Locate every blood parasite and identify its species.
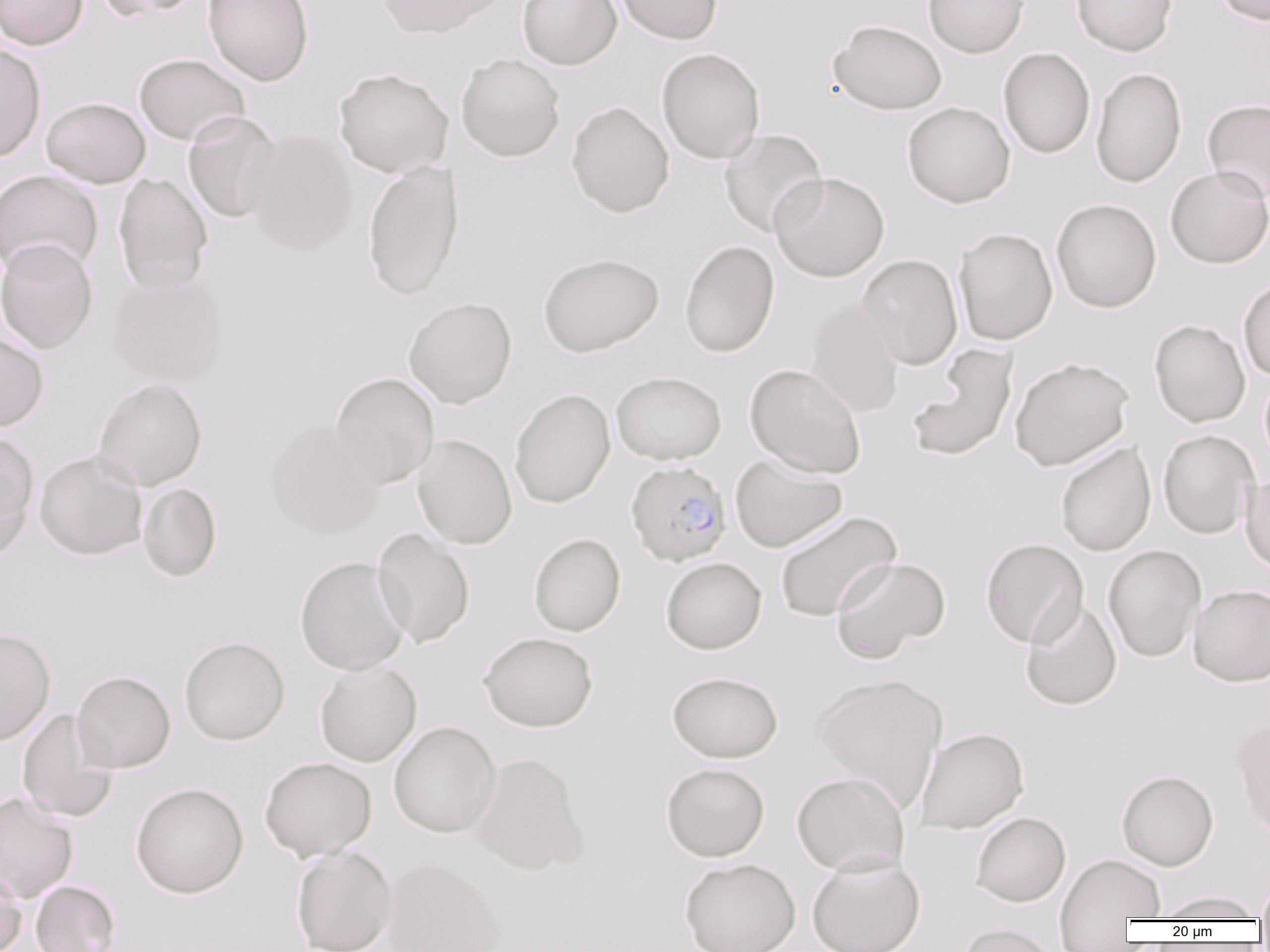

Approximate bounding boxes as named x1/y1/x2/y2 corners in pixels.
Plasmodium falciparum-infected red blood cells: (x1=625, y1=460, x2=732, y2=566).
No Plasmodium ovale, Plasmodium malariae, Plasmodium vivax, Babesia divergens, or Trypanosoma brucei observed.

Uninfected red blood cell locations: (x1=0, y1=0, x2=87, y2=50), (x1=94, y1=0, x2=204, y2=21), (x1=202, y1=0, x2=315, y2=86), (x1=376, y1=0, x2=503, y2=38), (x1=517, y1=0, x2=622, y2=70), (x1=612, y1=0, x2=723, y2=44), (x1=923, y1=0, x2=1029, y2=58), (x1=1071, y1=0, x2=1178, y2=56), (x1=1212, y1=0, x2=1270, y2=26), (x1=828, y1=19, x2=947, y2=114), (x1=0, y1=43, x2=46, y2=163), (x1=656, y1=47, x2=766, y2=164), (x1=998, y1=47, x2=1095, y2=159), (x1=134, y1=53, x2=250, y2=145), (x1=455, y1=54, x2=566, y2=162), (x1=1090, y1=67, x2=1187, y2=188), (x1=333, y1=68, x2=453, y2=178), (x1=41, y1=97, x2=150, y2=188), (x1=1202, y1=98, x2=1270, y2=203), (x1=566, y1=101, x2=675, y2=218), (x1=902, y1=102, x2=1015, y2=208), (x1=183, y1=111, x2=283, y2=223), (x1=245, y1=128, x2=357, y2=256), (x1=719, y1=129, x2=828, y2=237), (x1=362, y1=159, x2=464, y2=300), (x1=1164, y1=167, x2=1270, y2=269), (x1=0, y1=169, x2=103, y2=278), (x1=770, y1=171, x2=890, y2=281), (x1=113, y1=173, x2=213, y2=294), (x1=1051, y1=198, x2=1162, y2=313), (x1=953, y1=228, x2=1058, y2=346), (x1=0, y1=238, x2=99, y2=354), (x1=679, y1=240, x2=779, y2=358), (x1=537, y1=252, x2=664, y2=357), (x1=857, y1=254, x2=963, y2=370), (x1=106, y1=273, x2=229, y2=386), (x1=1238, y1=278, x2=1270, y2=381), (x1=404, y1=297, x2=517, y2=408), (x1=805, y1=298, x2=904, y2=418), (x1=1148, y1=319, x2=1250, y2=427), (x1=0, y1=332, x2=49, y2=432), (x1=906, y1=344, x2=1019, y2=462), (x1=1009, y1=356, x2=1134, y2=471), (x1=744, y1=364, x2=867, y2=478), (x1=611, y1=370, x2=727, y2=464), (x1=331, y1=372, x2=440, y2=489), (x1=93, y1=378, x2=207, y2=490), (x1=509, y1=389, x2=616, y2=508), (x1=264, y1=419, x2=385, y2=538), (x1=0, y1=430, x2=39, y2=554), (x1=1158, y1=430, x2=1259, y2=539), (x1=412, y1=434, x2=517, y2=549), (x1=1055, y1=442, x2=1156, y2=556), (x1=35, y1=450, x2=148, y2=560), (x1=730, y1=454, x2=848, y2=553), (x1=1241, y1=473, x2=1270, y2=575), (x1=138, y1=483, x2=222, y2=582), (x1=774, y1=511, x2=901, y2=622), (x1=372, y1=528, x2=475, y2=648), (x1=529, y1=533, x2=625, y2=636), (x1=980, y1=538, x2=1088, y2=648), (x1=1103, y1=544, x2=1206, y2=662), (x1=294, y1=556, x2=410, y2=675), (x1=830, y1=556, x2=951, y2=662), (x1=660, y1=557, x2=766, y2=654), (x1=1188, y1=584, x2=1270, y2=686), (x1=1020, y1=599, x2=1122, y2=710), (x1=0, y1=628, x2=55, y2=747), (x1=479, y1=632, x2=598, y2=732), (x1=179, y1=636, x2=290, y2=746), (x1=314, y1=661, x2=422, y2=766), (x1=71, y1=670, x2=176, y2=773), (x1=667, y1=671, x2=783, y2=762), (x1=813, y1=673, x2=947, y2=810), (x1=17, y1=708, x2=118, y2=823), (x1=1229, y1=715, x2=1270, y2=839), (x1=388, y1=721, x2=501, y2=838), (x1=916, y1=727, x2=1029, y2=834), (x1=469, y1=752, x2=590, y2=875), (x1=259, y1=756, x2=377, y2=861), (x1=661, y1=762, x2=770, y2=861), (x1=1116, y1=770, x2=1219, y2=871), (x1=791, y1=771, x2=909, y2=875), (x1=130, y1=781, x2=249, y2=898), (x1=0, y1=792, x2=79, y2=903), (x1=971, y1=812, x2=1071, y2=907), (x1=290, y1=845, x2=397, y2=952), (x1=1054, y1=852, x2=1164, y2=945), (x1=807, y1=854, x2=925, y2=952), (x1=381, y1=857, x2=504, y2=952), (x1=680, y1=858, x2=800, y2=952), (x1=0, y1=869, x2=26, y2=952), (x1=1256, y1=874, x2=1270, y2=922), (x1=30, y1=880, x2=121, y2=952), (x1=1154, y1=890, x2=1265, y2=921), (x1=957, y1=923, x2=1060, y2=952). Slide-level diagnosis: Plasmodium falciparum. 1000x magnification. Thin blood film. Optical microscopy. One field of a larger specimen. Image is 1270×952 pixels.